Identify the parasite.
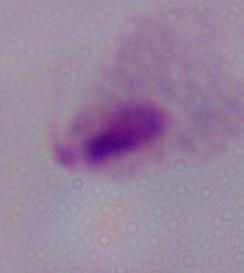

A trichomonad.

Summary:
  - Magnification: 1000x
  - Modality: photomicrograph